Locate and identify every blood parasite.
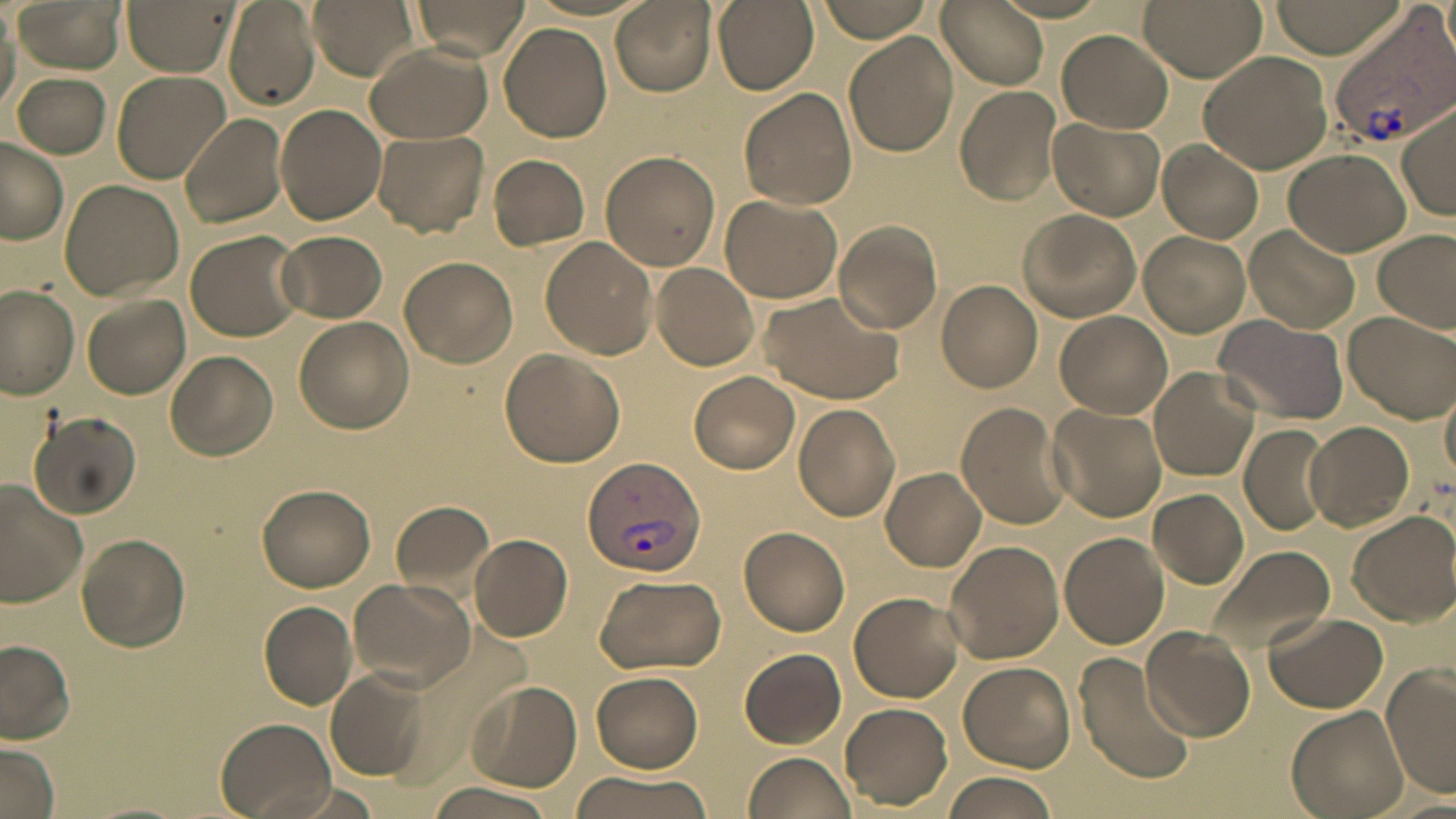

Approximate bounding boxes as (x1,y1)-(x2,y2) corner pairs in pixels.
Plasmodium vivax-infected red blood cells: (1329,6)-(1456,148), (582,454)-(706,576).
No Plasmodium falciparum, Plasmodium ovale, Plasmodium malariae, Babesia divergens, or Trypanosoma brucei observed.

{
  "slide_level_diagnosis": "Plasmodium vivax",
  "uninfected_red_blood_cell_locations": "approximate bounding boxes as (x1,y1)-(x2,y2) corner pairs in pixels: (14,0)-(127,73), (123,0)-(237,75), (308,0)-(417,80), (408,0)-(530,60), (611,0)-(714,95), (711,0)-(820,93), (815,0)-(936,42), (937,0)-(1051,92), (1139,0)-(1266,80), (1268,0)-(1407,57), (224,1)-(319,112), (498,22)-(612,143), (1058,31)-(1173,133), (843,32)-(958,156), (366,43)-(492,143), (1198,48)-(1337,174), (112,70)-(230,183), (13,72)-(111,157), (956,86)-(1062,205), (737,87)-(857,210), (275,103)-(388,225), (1398,104)-(1455,221), (180,113)-(288,228), (1047,117)-(1165,221), (371,131)-(489,237), (0,138)-(68,245), (1156,141)-(1263,243), (1284,149)-(1410,257), (600,151)-(721,271), (489,155)-(590,250), (59,180)-(182,299), (720,194)-(842,303), (1018,209)-(1142,323), (831,220)-(942,334), (1243,226)-(1359,335), (1373,228)-(1455,332), (185,229)-(308,343), (274,229)-(388,323), (1139,232)-(1251,337), (539,236)-(659,360), (401,257)-(517,367), (649,262)-(760,371), (936,279)-(1043,393), (1,286)-(81,400), (759,290)-(906,402), (83,295)-(191,399), (1055,310)-(1172,418), (1344,310)-(1454,423), (1213,314)-(1349,425), (295,317)-(415,435), (498,347)-(625,468), (165,350)-(278,460), (1148,366)-(1259,480), (688,370)-(799,473), (1441,381)-(1456,487), (793,402)-(900,521), (955,402)-(1071,530), (1047,404)-(1168,522), (32,414)-(142,517), (1303,420)-(1414,532), (1239,423)-(1334,537), (881,467)-(987,571), (0,482)-(90,606), (257,483)-(377,592), (1149,488)-(1249,588), (388,497)-(496,603), (1349,511)-(1456,625), (739,526)-(849,636), (1059,531)-(1169,649), (466,533)-(574,642), (76,534)-(191,653), (943,540)-(1065,664), (1201,546)-(1336,660), (592,574)-(726,675), (346,578)-(475,691), (850,593)-(963,701), (258,601)-(359,709), (1263,612)-(1388,714), (1141,627)-(1255,740), (0,638)-(76,743), (739,648)-(846,749), (1075,651)-(1197,786), (958,661)-(1076,771), (1382,662)-(1456,801), (325,666)-(435,780), (591,671)-(703,772), (462,680)-(583,792), (841,704)-(951,808), (1287,705)-(1408,819), (216,718)-(335,819), (1,744)-(60,819), (741,752)-(858,819), (569,772)-(717,818), (943,773)-(1058,819), (423,780)-(562,819)",
  "field_of_view": "single",
  "preparation": "thin blood film",
  "magnification": "1000x",
  "image_size": "1456×819 pixels",
  "modality": "light microscopy",
  "stain": "May-Grünwald-Giemsa"
}